Give the extent of all Plasmodium vivax-infected red blood cells.
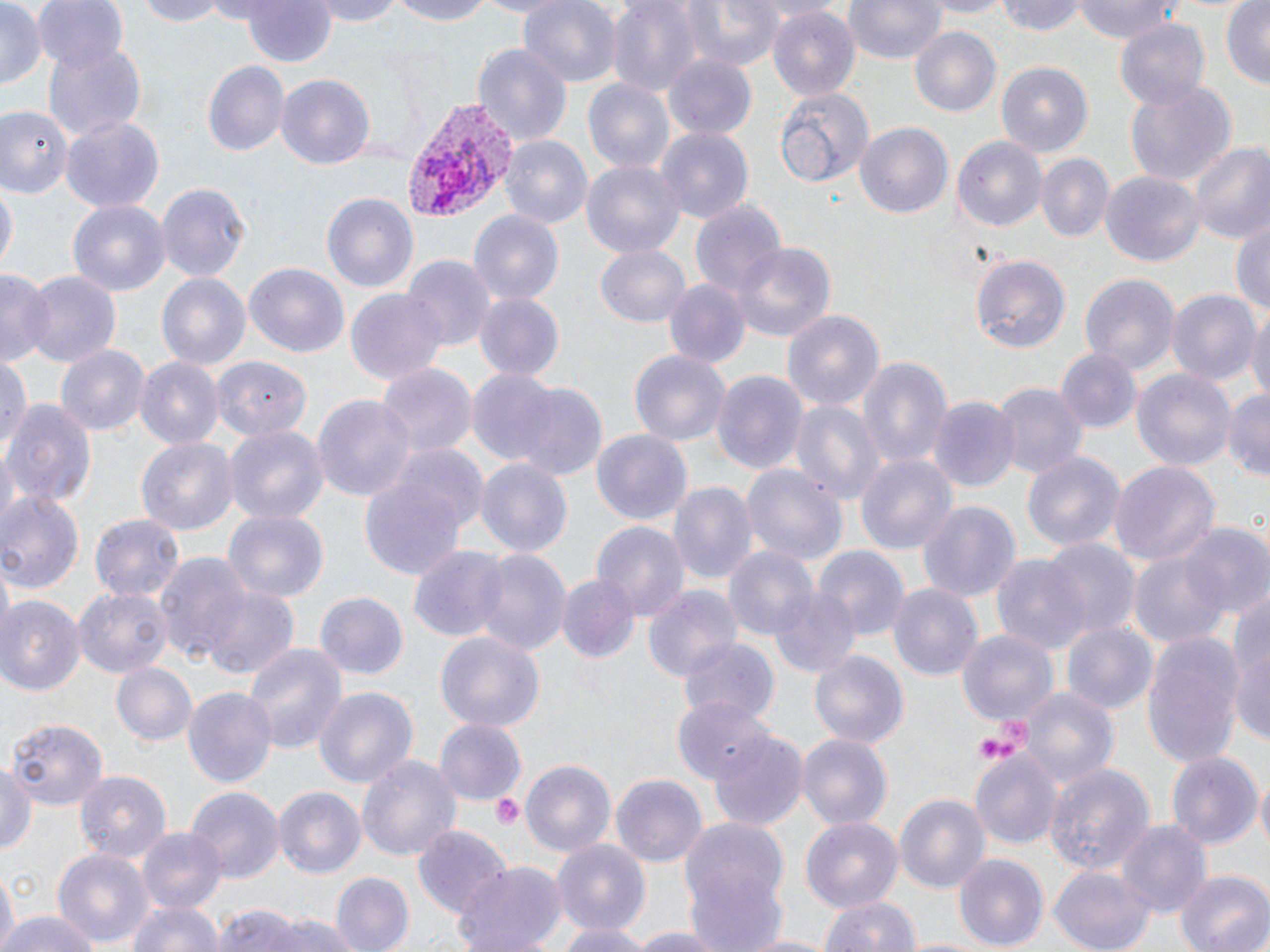

Approximate bounding boxes as [x1, y1, x2, y2] in pixels.
Plasmodium vivax-infected red blood cells: [399, 97, 521, 220].

{
  "slide_level_diagnosis": "Plasmodium vivax",
  "field_of_view": "one of a larger specimen",
  "stain": "May-Grünwald-Giemsa",
  "platelet_locations": "approximate bounding boxes as [x1, y1, x2, y2] in pixels: [971, 731, 1019, 767], [488, 791, 525, 829]",
  "modality": "light microscopy",
  "image_size": "1270×952 pixels",
  "magnification": "1000x",
  "uninfected_red_blood_cell_locations": "approximate bounding boxes as [x1, y1, x2, y2] in pixels: [0, 0, 44, 92], [34, 0, 130, 74], [136, 0, 229, 27], [306, 0, 411, 25], [380, 0, 500, 25], [519, 0, 622, 88], [609, 0, 701, 95], [672, 0, 786, 71], [840, 0, 950, 64], [918, 0, 1014, 16], [995, 0, 1090, 36], [1073, 0, 1192, 47], [1220, 0, 1269, 91], [243, 2, 339, 70], [768, 7, 861, 101], [1115, 18, 1211, 107], [910, 26, 1004, 118], [41, 41, 148, 141], [473, 44, 573, 144], [663, 56, 756, 139], [202, 60, 289, 157], [996, 62, 1094, 155], [276, 74, 373, 171], [582, 77, 674, 172], [1124, 82, 1235, 189], [772, 84, 876, 191], [0, 106, 74, 196], [62, 117, 165, 212], [856, 123, 952, 221], [656, 126, 752, 224], [499, 135, 592, 229], [952, 136, 1045, 233], [1186, 141, 1270, 245], [1036, 155, 1113, 244], [580, 159, 686, 259], [1101, 171, 1203, 265], [156, 180, 249, 284], [0, 182, 16, 275], [322, 192, 419, 292], [67, 199, 171, 294], [692, 202, 787, 304], [468, 210, 563, 306], [1232, 217, 1269, 319], [731, 242, 834, 342], [594, 243, 691, 327], [971, 254, 1071, 352], [401, 255, 494, 350], [245, 263, 349, 358], [1, 267, 50, 368], [22, 268, 121, 365], [1081, 273, 1179, 374], [155, 274, 250, 370], [662, 279, 751, 370], [1167, 289, 1259, 387], [345, 290, 449, 384], [473, 293, 564, 380], [782, 309, 883, 418], [1246, 310, 1270, 410], [55, 345, 150, 438], [1056, 349, 1143, 435], [628, 350, 730, 446], [857, 353, 952, 473], [0, 356, 29, 455], [213, 357, 310, 438], [135, 358, 224, 449], [375, 364, 477, 459], [1134, 367, 1236, 476], [487, 368, 596, 528], [466, 369, 565, 467], [712, 370, 808, 479], [991, 384, 1087, 484], [511, 385, 607, 482], [1219, 386, 1270, 480], [313, 395, 416, 502], [929, 396, 1020, 491], [3, 398, 96, 508], [789, 398, 883, 508], [225, 423, 329, 525], [590, 428, 692, 527], [137, 436, 239, 538], [386, 444, 493, 538], [1021, 449, 1125, 556], [856, 454, 959, 553], [474, 458, 573, 558], [1109, 458, 1220, 567], [742, 464, 847, 569], [357, 467, 473, 582], [669, 481, 756, 587], [1, 489, 84, 591], [917, 501, 1018, 601], [222, 507, 328, 600], [88, 513, 184, 605], [591, 520, 690, 619], [1181, 524, 1270, 616], [1039, 538, 1139, 642], [723, 543, 819, 640], [408, 545, 511, 642], [815, 545, 908, 641], [471, 547, 569, 658], [1128, 549, 1232, 651], [156, 552, 256, 664], [992, 553, 1086, 652], [556, 574, 639, 663], [197, 582, 300, 683], [887, 582, 984, 680], [644, 583, 742, 682], [768, 584, 862, 679], [72, 586, 170, 679], [314, 591, 407, 679], [1227, 591, 1270, 746], [0, 597, 83, 695], [1192, 616, 1263, 759], [1060, 620, 1158, 716], [957, 629, 1056, 725], [1142, 631, 1243, 770], [435, 633, 544, 730], [680, 639, 776, 724], [242, 640, 347, 757], [807, 648, 910, 749], [112, 663, 197, 745], [314, 684, 418, 791], [183, 686, 277, 790], [1022, 688, 1119, 786], [671, 697, 773, 785], [6, 716, 107, 810], [434, 719, 526, 807], [709, 729, 809, 828], [798, 735, 891, 831], [973, 751, 1064, 848], [1167, 751, 1262, 853], [355, 752, 462, 863], [518, 759, 618, 857], [1043, 761, 1156, 877], [2, 763, 40, 860], [74, 769, 170, 860], [1254, 773, 1270, 855], [611, 774, 706, 866], [274, 786, 366, 880], [185, 788, 281, 883], [895, 794, 992, 894], [677, 816, 789, 946], [800, 817, 904, 917], [1119, 821, 1212, 918], [413, 824, 513, 917], [137, 827, 227, 915], [550, 838, 651, 935], [54, 849, 152, 950], [952, 854, 1048, 948], [453, 861, 568, 952], [1050, 867, 1155, 951], [1175, 868, 1270, 952], [0, 869, 24, 942], [332, 872, 414, 952], [819, 894, 920, 952], [124, 897, 224, 952], [213, 905, 312, 952], [0, 911, 101, 952], [270, 913, 359, 952], [555, 919, 655, 952], [619, 926, 733, 952], [734, 931, 841, 952]",
  "preparation": "thin blood film"
}